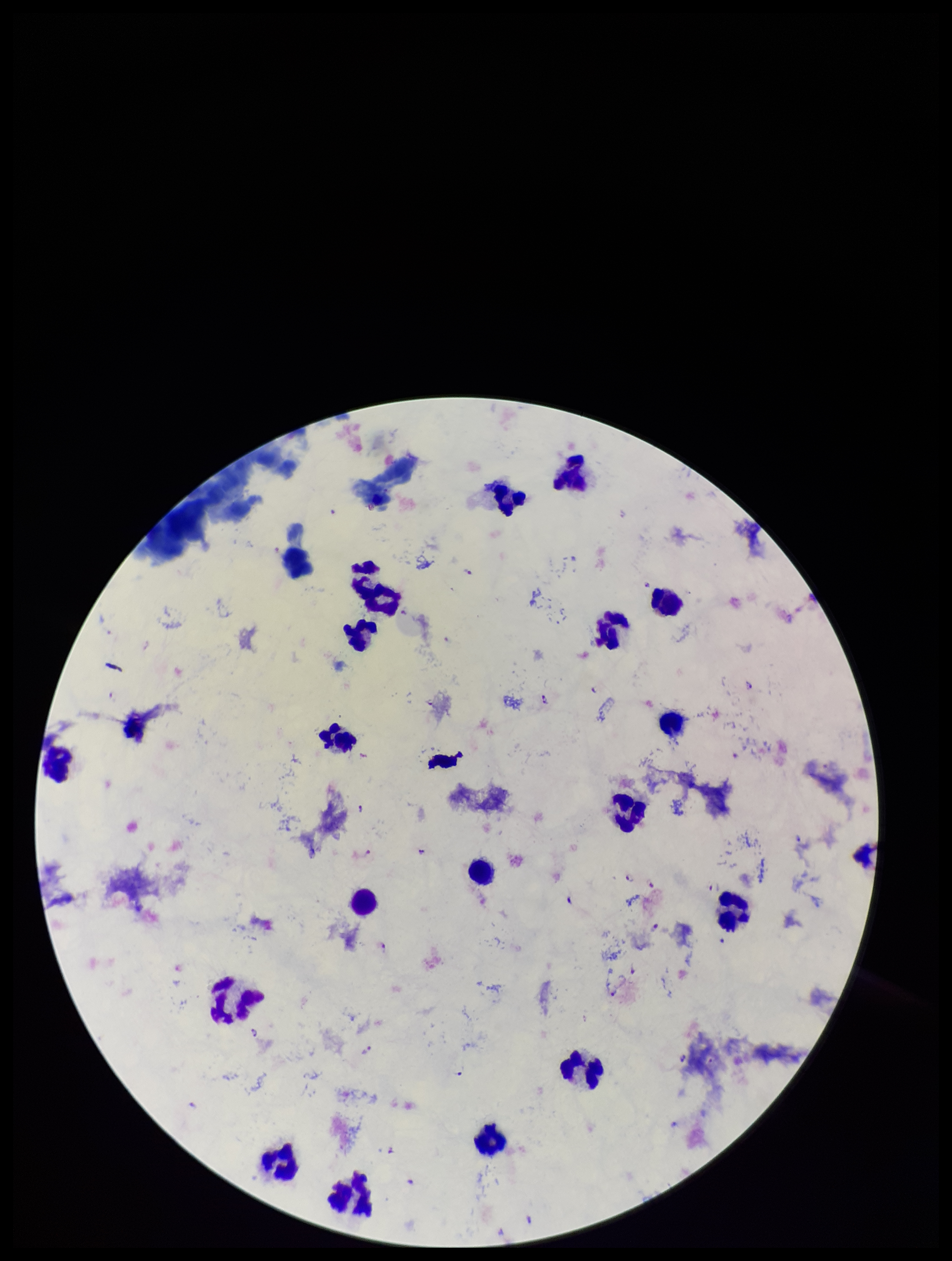
{
  "image_size": "952×1261 pixels",
  "parasite_count": 21,
  "capture": "smartphone photograph through the microscope eyepiece",
  "species_reported_for_this_patient": "Plasmodium falciparum",
  "patient_malaria_status": "positive",
  "leukocyte_count": 19,
  "plasmodium_parasites": "identified",
  "preparation": "thick blood smear",
  "field_of_view": "single",
  "stain": "Giemsa"
}